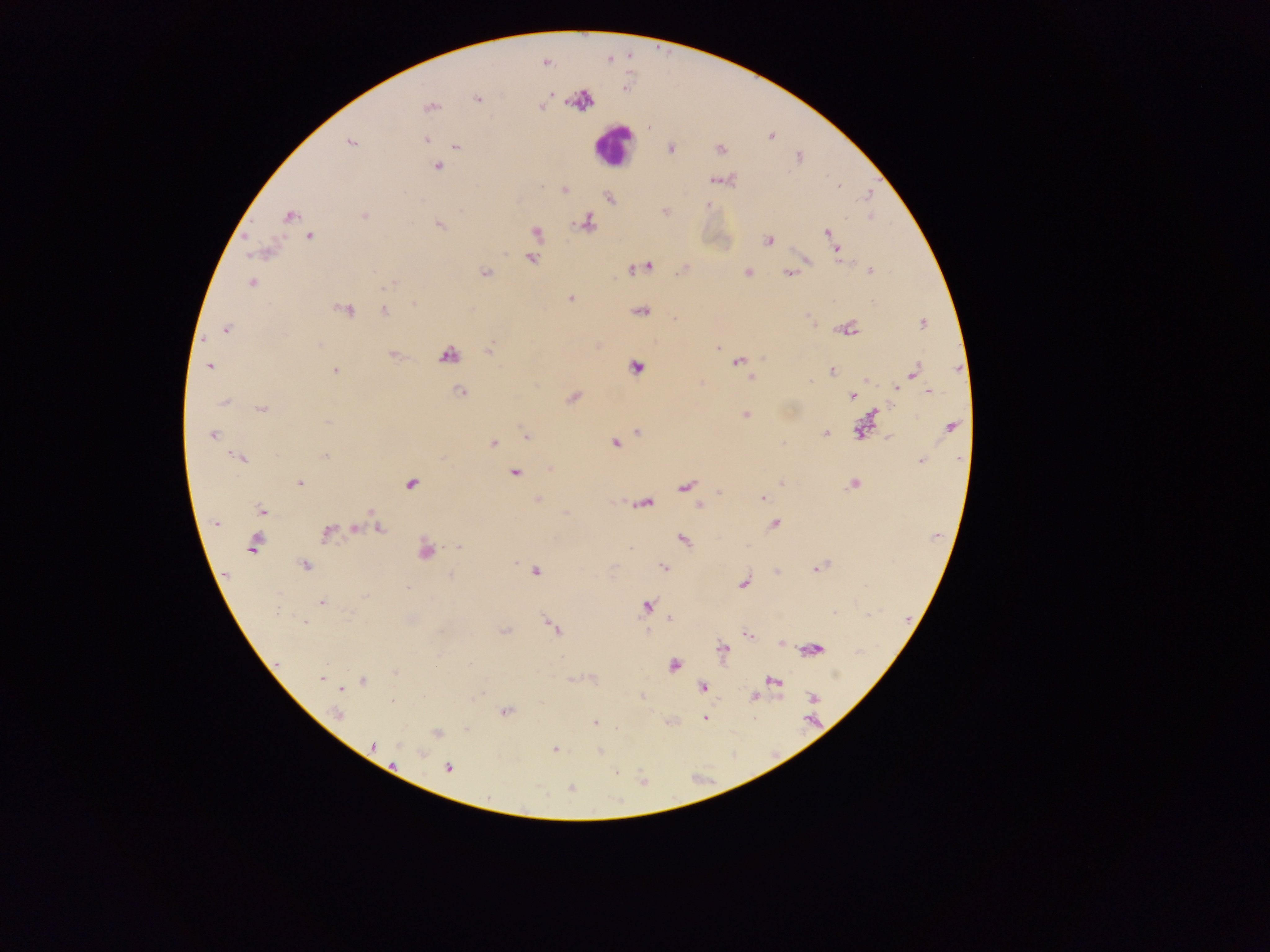
Approximate centers as (x, y) in pixels.
Summary:
  - Leukocyte locations: (612, 143)
  - Malaria parasite locations: (545, 63), (477, 98), (429, 106), (542, 106), (648, 128), (772, 136), (426, 139), (351, 142), (457, 146), (670, 148), (720, 150), (799, 157), (437, 166), (715, 180), (838, 185), (565, 191), (868, 193), (609, 197), (709, 205), (664, 212), (289, 215), (364, 215), (587, 224), (439, 225), (537, 232), (827, 232), (310, 237), (768, 240), (837, 249), (267, 251), (531, 257), (648, 265), (870, 271), (486, 273), (748, 273), (788, 274), (251, 283), (389, 284), (570, 299), (414, 304), (347, 310), (641, 310), (385, 311), (807, 317), (923, 323), (847, 329), (226, 330), (489, 348), (717, 348), (447, 354), (392, 355), (763, 358), (738, 362), (209, 366), (636, 367), (335, 371), (831, 371), (914, 371), (750, 377), (867, 380), (896, 389), (459, 391), (929, 392), (852, 396), (573, 397), (223, 402), (261, 410), (746, 414), (327, 421), (950, 426), (859, 431), (638, 432), (826, 434), (212, 435), (525, 436), (888, 437), (615, 443), (782, 443), (493, 444), (325, 456), (240, 458), (921, 460), (515, 472), (300, 482), (411, 483), (781, 483), (853, 484), (685, 486), (720, 492), (538, 499), (762, 499), (646, 503), (699, 505), (262, 510), (216, 524), (775, 524), (378, 528), (355, 529), (326, 533), (683, 539), (254, 545), (459, 547), (629, 548), (425, 551), (515, 562), (304, 565), (664, 568), (816, 569), (537, 571), (449, 576), (743, 582), (407, 588), (365, 596), (320, 602), (646, 606), (276, 612), (350, 612), (834, 612), (671, 619), (304, 622), (553, 627), (505, 630), (748, 634), (780, 643), (723, 649), (673, 665), (395, 672), (321, 679), (363, 681), (774, 681), (702, 686), (340, 689), (642, 696), (755, 696), (813, 696), (393, 701), (506, 711), (337, 714), (705, 719), (595, 722), (466, 728), (436, 733), (372, 746), (555, 749), (599, 751), (421, 753), (447, 767), (615, 772), (570, 788)
  - Preparation: thick blood smear
  - Field of view: single
  - Capture: mobile-phone photograph through a microscope
  - Country: Ghana
  - Image size: 1270×952 pixels